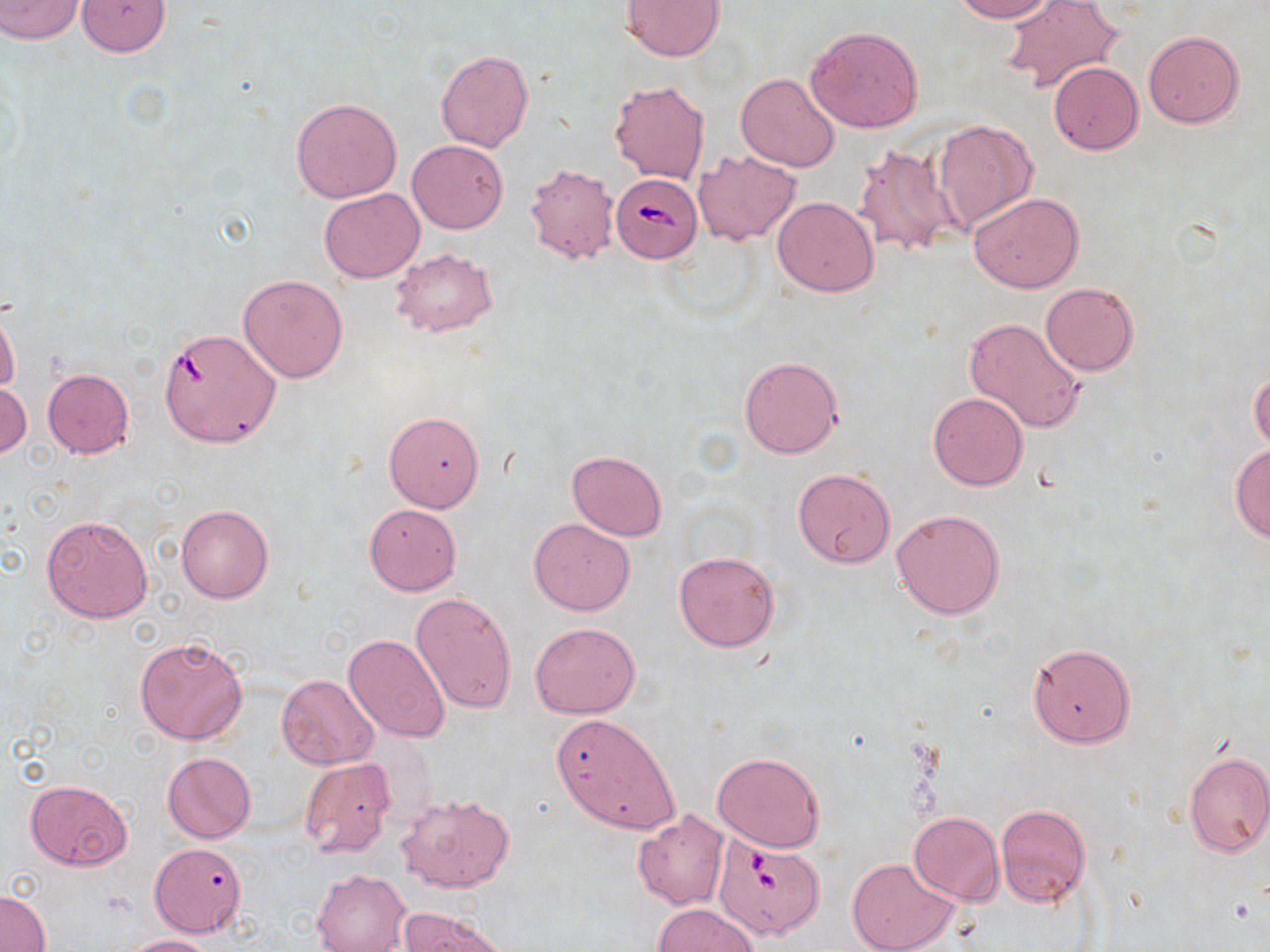
Summary:
  - Coordinate format: approximate bounding boxes as [x1, y1, x2, y2] in pixels
  - Uninfected red blood cell locations: [0, 0, 83, 42], [77, 0, 171, 56], [622, 0, 724, 60], [951, 0, 1058, 22], [1003, 1, 1123, 93], [806, 25, 924, 132], [1143, 29, 1245, 128], [437, 50, 532, 152], [1049, 61, 1143, 154], [736, 72, 840, 172], [610, 80, 709, 184], [290, 97, 402, 203], [931, 119, 1037, 233], [407, 140, 507, 233], [853, 143, 961, 258], [694, 150, 800, 244], [524, 163, 619, 265], [320, 188, 425, 282], [968, 192, 1084, 293], [773, 197, 877, 296], [390, 247, 497, 340], [239, 275, 348, 382], [1040, 283, 1139, 375], [0, 304, 20, 396], [963, 317, 1085, 434], [157, 333, 293, 450], [738, 357, 843, 459], [43, 368, 134, 458], [1249, 368, 1270, 453], [0, 382, 31, 459], [928, 392, 1028, 491], [383, 409, 485, 512], [1228, 443, 1270, 544], [567, 450, 667, 541], [793, 467, 895, 569], [364, 503, 461, 594], [176, 504, 273, 602], [891, 508, 1005, 620], [41, 513, 153, 623], [529, 518, 634, 614], [673, 551, 779, 652], [410, 592, 516, 714], [531, 621, 641, 718], [345, 634, 450, 744], [134, 635, 248, 746], [1028, 643, 1135, 747], [277, 674, 378, 769], [550, 713, 679, 834], [1182, 749, 1270, 858], [712, 751, 826, 853], [163, 752, 255, 843], [300, 757, 395, 858], [24, 780, 132, 869], [397, 793, 514, 894], [995, 804, 1090, 908], [633, 809, 730, 909], [909, 812, 1004, 905], [150, 843, 246, 936], [847, 857, 960, 952], [312, 869, 411, 952], [1, 889, 50, 951], [653, 903, 759, 952], [398, 909, 503, 952], [121, 935, 216, 952]
  - Babesia divergens-infected red blood cell locations: [612, 172, 702, 262], [713, 834, 826, 940]
  - Slide-level diagnosis: Babesia divergens
  - Magnification: 1000x
  - Modality: light microscopy
  - Preparation: thin blood film
  - Stain: May-Grünwald-Giemsa
  - Image size: 1270×952 pixels
  - Field of view: single